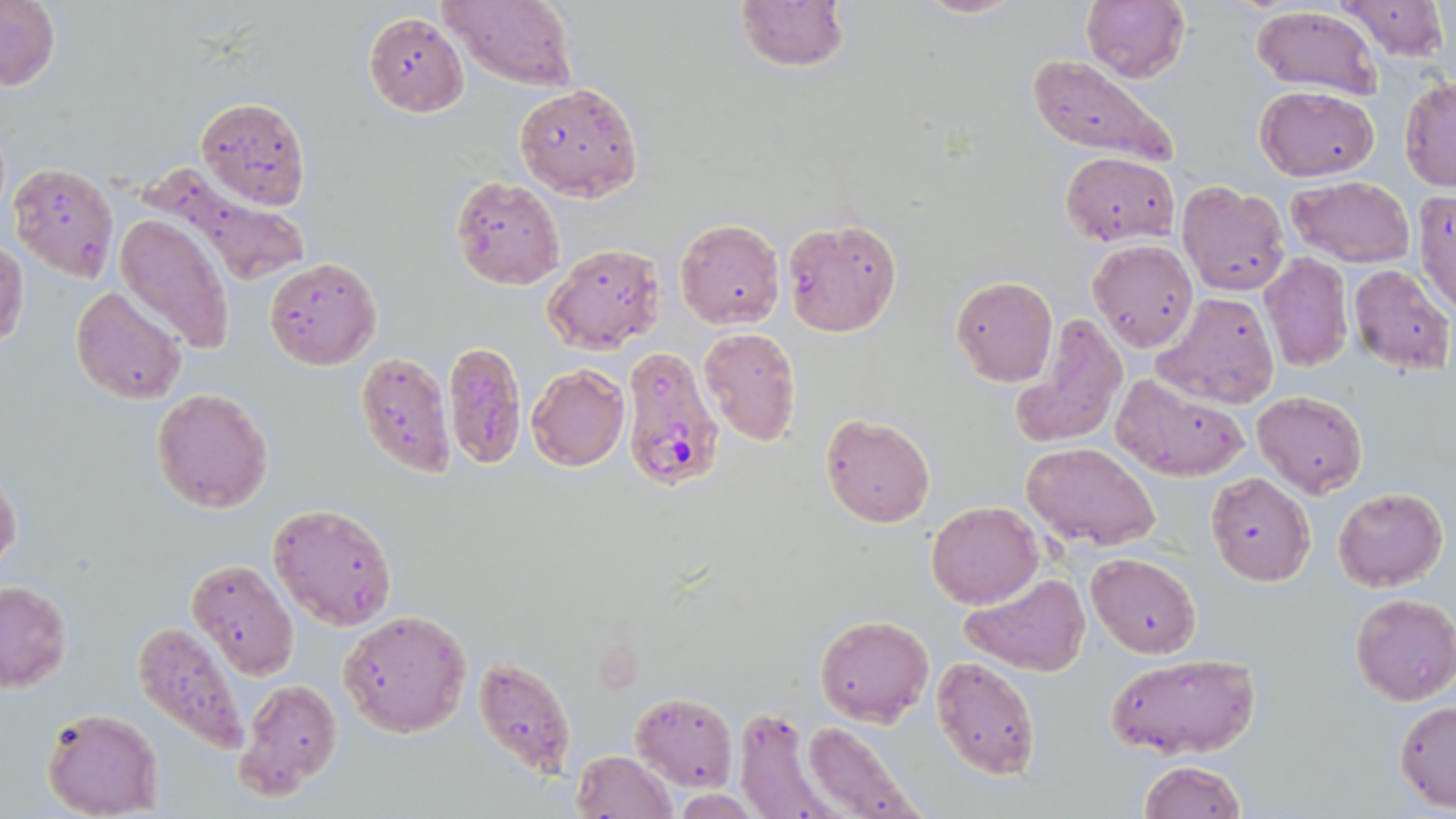

{
  "plasmodium_falciparum_infected_red_blood_cell_locations": "approximate bounding boxes as (x1, y1, x2, y2) in pixels: (621, 345, 723, 491)",
  "slide_level_diagnosis": "Plasmodium falciparum",
  "stain": "May-Grünwald-Giemsa",
  "preparation": "thin blood film",
  "modality": "light microscopy",
  "image_size": "1456×819 pixels",
  "uninfected_red_blood_cell_locations": "approximate bounding boxes as (x1, y1, x2, y2) in pixels: (0, 0, 59, 91), (440, 0, 577, 91), (734, 0, 849, 73), (912, 0, 1025, 19), (1083, 0, 1191, 84), (1334, 0, 1452, 63), (1251, 4, 1384, 100), (364, 13, 468, 117), (1026, 57, 1178, 166), (1400, 75, 1456, 190), (513, 81, 644, 202), (1256, 85, 1380, 180), (196, 97, 310, 208), (1059, 150, 1180, 246), (9, 163, 118, 281), (1287, 175, 1417, 268), (451, 176, 564, 289), (1177, 182, 1291, 295), (1413, 188, 1455, 319), (115, 212, 235, 352), (676, 217, 784, 331), (781, 217, 902, 338), (1088, 239, 1197, 352), (0, 242, 27, 349), (544, 243, 667, 354), (1259, 253, 1354, 373), (264, 256, 383, 369), (1348, 264, 1453, 375), (951, 276, 1057, 386), (72, 286, 187, 404), (1154, 291, 1280, 407), (1008, 316, 1127, 447), (699, 328, 801, 445), (443, 341, 526, 468), (355, 353, 455, 480), (527, 364, 629, 470), (1111, 372, 1249, 482), (152, 388, 273, 513), (1251, 391, 1369, 498), (821, 413, 935, 528), (1022, 442, 1162, 551), (1206, 472, 1315, 586), (0, 476, 22, 571), (1333, 487, 1447, 591), (269, 501, 399, 630), (926, 501, 1044, 609), (1086, 552, 1201, 658), (188, 559, 298, 678), (961, 571, 1093, 678), (0, 581, 72, 692), (1349, 593, 1456, 705), (340, 609, 472, 738), (815, 613, 933, 727), (133, 621, 250, 755), (1105, 653, 1262, 760), (474, 656, 578, 784), (930, 656, 1042, 781), (235, 681, 343, 801), (631, 692, 738, 791), (1394, 700, 1456, 812), (734, 707, 836, 819), (41, 708, 163, 819), (799, 721, 924, 819), (571, 749, 676, 818), (1137, 759, 1248, 818), (671, 790, 761, 818)",
  "field_of_view": "single",
  "magnification": "1000x"
}